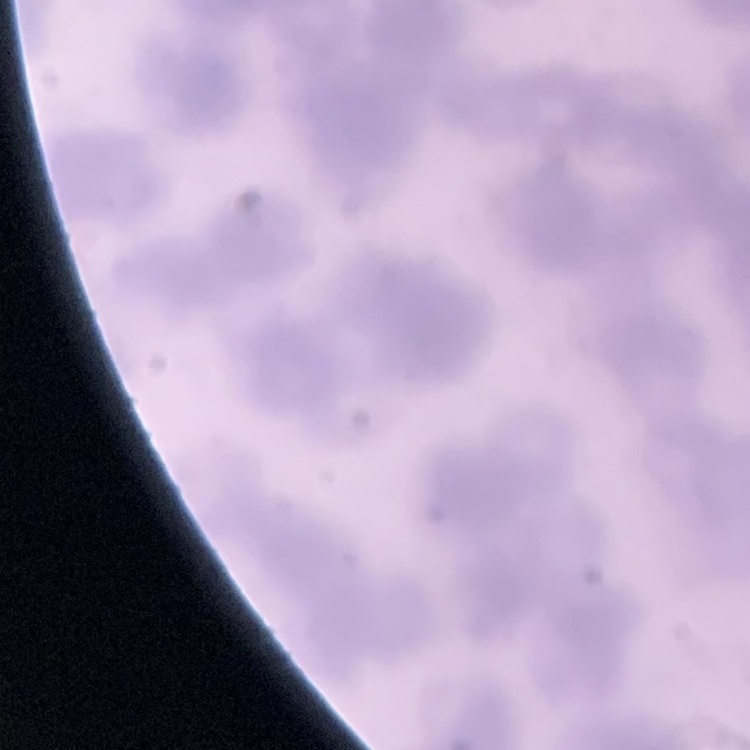

Summary:
  - Erythrocyte morphology: rouleaux formation
  - Stain: Field's or Giemsa
  - Preparation: thin blood film
  - Image type: square crop of a larger photomicrograph